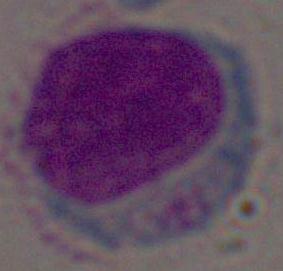

identification: leukocyte
magnification: 1000x
modality: micrograph